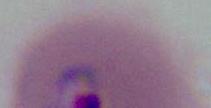
{
  "identification": "Plasmodium",
  "magnification": "400x or 1000x",
  "modality": "photomicrograph"
}